Evaluate for malaria.
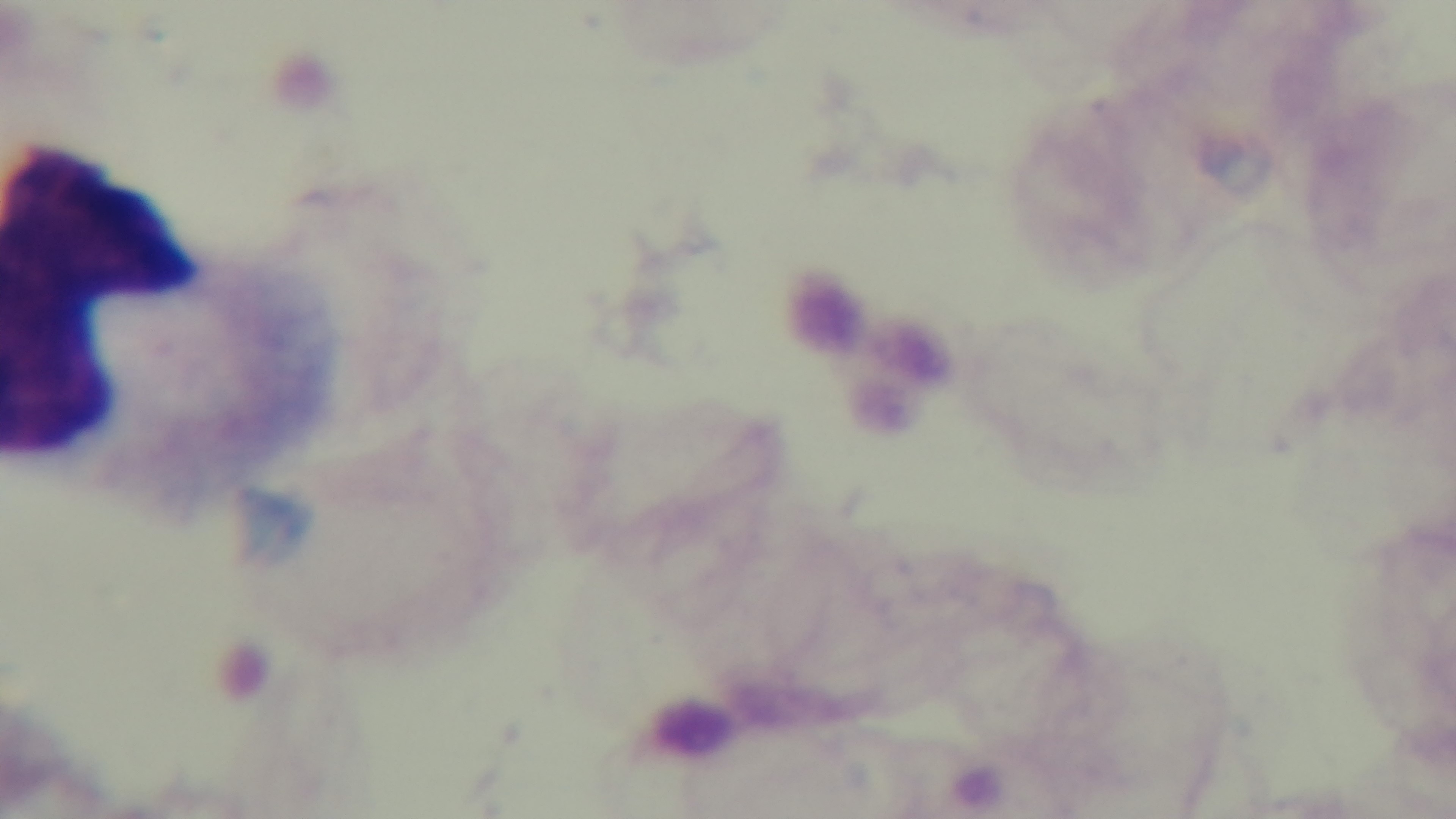

Negative.

100x oil-immersion objective. Mounted 4K digital camera. Light microscopy. One field from the slide. Giemsa stain. Preparation: thick.